Describe the morphology of the red blood cells.
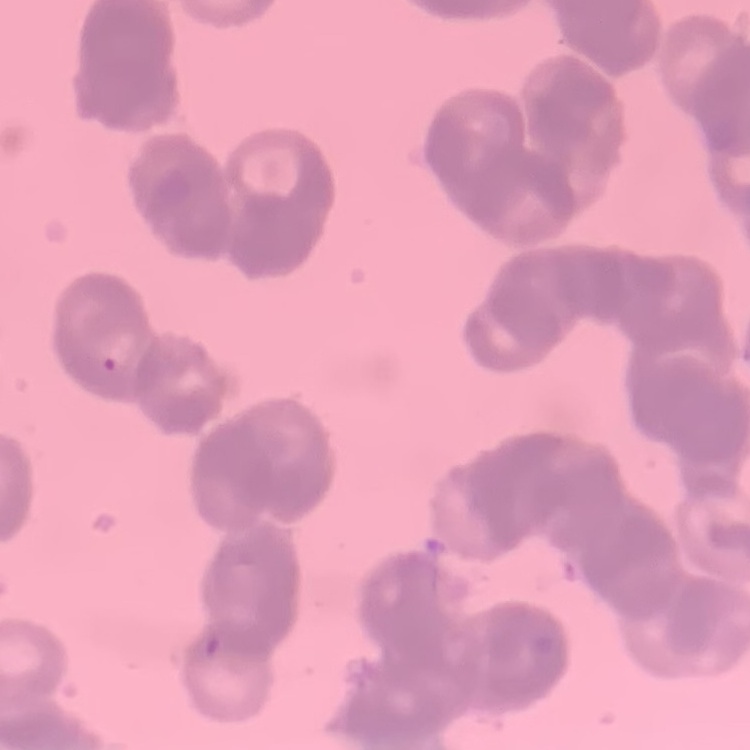

They show rouleaux formation.

{
  "image_type": "square crop of a larger photomicrograph",
  "stain": "Field's or Giemsa",
  "preparation": "thin blood film"
}